Name the parasite shown.
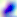
Toxoplasma gondii.

Captured at 400x magnification. Photomicrograph.